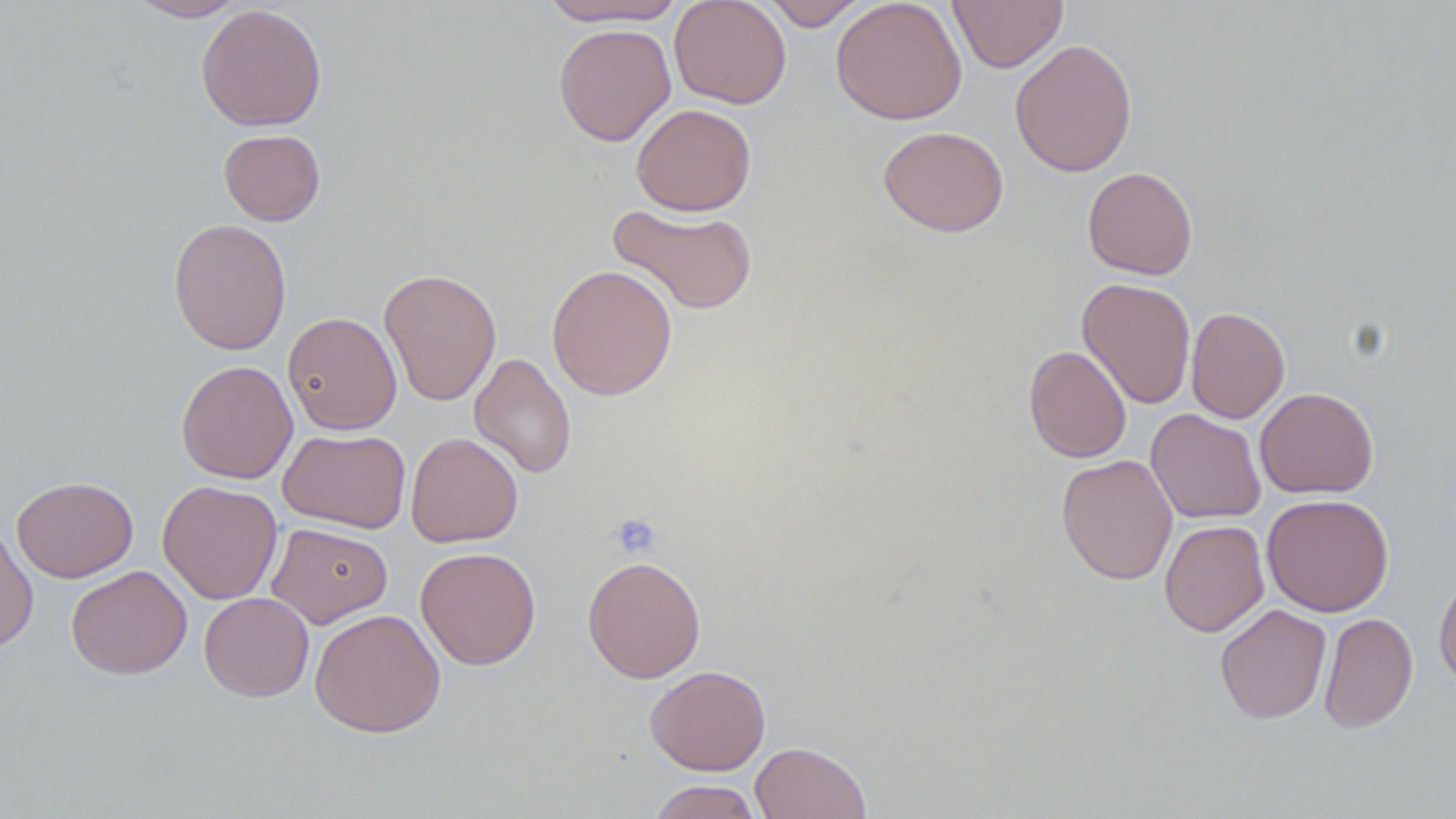

slide-level diagnosis = no evidence of blood parasites
stain = May-Grünwald-Giemsa
field of view = one of a larger specimen
modality = light microscopy
preparation = thin blood film
magnification = 1000x
image size = 1456×819 pixels
platelet locations = approximate bounding boxes as (x1,y1)-(x2,y2) corner pairs in pixels: (610,514)-(661,558)
uninfected red blood cell locations = approximate bounding boxes as (x1,y1)-(x2,y2) corner pairs in pixels: (126,0)-(250,22), (538,0)-(689,26), (668,0)-(792,109), (763,0)-(870,31), (831,0)-(967,125), (948,0)-(1068,73), (196,4)-(327,132), (553,23)-(676,146), (1010,38)-(1138,178), (631,103)-(757,216), (878,125)-(1009,237), (219,129)-(325,226), (1083,166)-(1198,280), (608,203)-(758,315), (168,218)-(292,355), (547,263)-(678,401), (378,268)-(502,406), (1078,277)-(1196,409), (1186,306)-(1290,423), (282,312)-(402,435), (1024,345)-(1132,463), (469,352)-(576,479), (176,359)-(298,484), (1255,387)-(1379,498), (1145,408)-(1266,524), (278,428)-(411,533), (406,432)-(523,548), (1056,454)-(1178,585), (11,476)-(138,583), (157,480)-(283,604), (1261,493)-(1394,616), (1159,519)-(1269,637), (0,520)-(38,655), (267,522)-(392,628), (415,547)-(541,670), (582,555)-(706,684), (66,564)-(192,680), (1434,572)-(1456,690), (199,592)-(315,702), (1215,604)-(1331,724), (309,608)-(446,737), (1318,612)-(1418,734), (645,665)-(771,775), (750,742)-(871,819), (647,779)-(765,819)